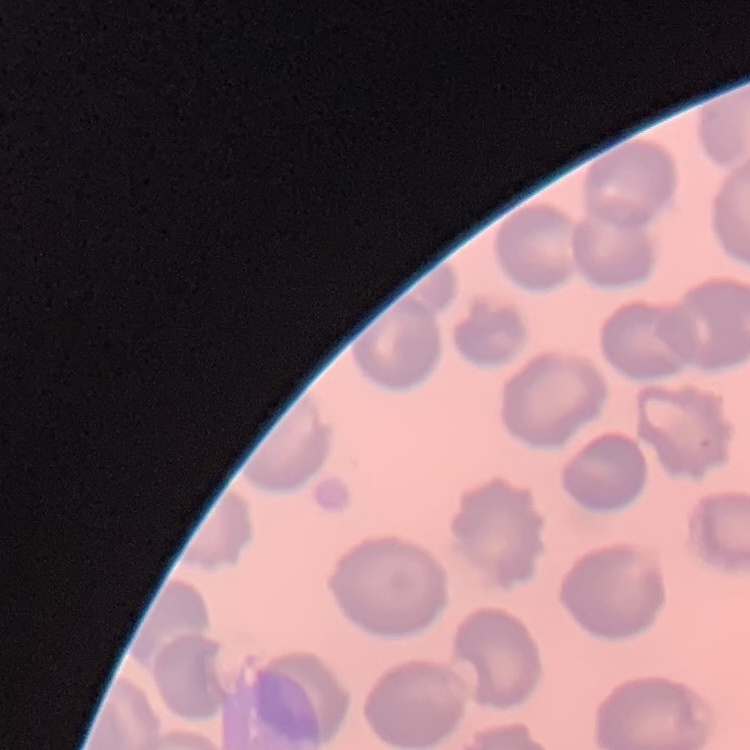
The erythrocytes show no rouleaux formation. Thin blood smear. One tile cut from a larger photomicrograph. Stained with either Field's or Giemsa.